Locate and identify every blood parasite.
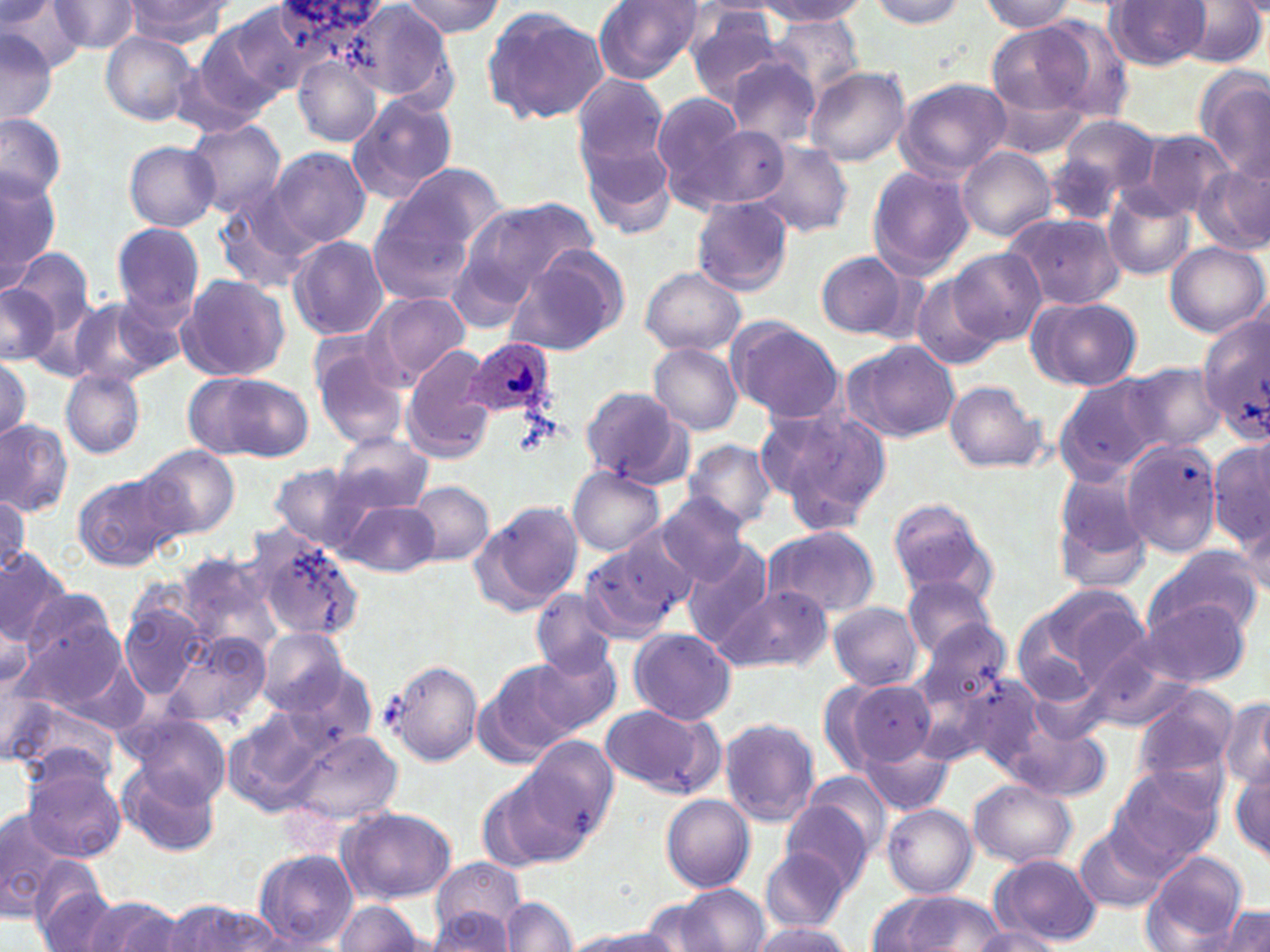

Approximate bounding boxes as [x1, y1, x2, y2] in pixels.
Plasmodium ovale-infected red blood cells: [466, 337, 557, 421].
No Plasmodium falciparum, Plasmodium malariae, Plasmodium vivax, Babesia divergens, or Trypanosoma brucei observed.

Uninfected red blood cell locations: [398, 0, 505, 37], [751, 0, 864, 35], [1106, 0, 1212, 70], [1178, 0, 1266, 69], [2, 1, 87, 74], [48, 1, 141, 56], [124, 1, 230, 46], [866, 1, 968, 29], [978, 1, 1080, 33], [271, 2, 388, 44], [592, 2, 704, 82], [220, 3, 325, 99], [349, 4, 455, 104], [481, 5, 610, 126], [684, 5, 790, 103], [768, 14, 864, 99], [1037, 15, 1138, 123], [196, 20, 295, 119], [985, 24, 1095, 131], [0, 30, 58, 126], [101, 32, 199, 125], [176, 44, 273, 138], [722, 55, 822, 148], [294, 56, 382, 149], [1194, 65, 1270, 181], [804, 66, 910, 168], [569, 72, 669, 177], [893, 77, 1011, 180], [347, 91, 458, 203], [653, 92, 756, 207], [0, 112, 66, 198], [577, 115, 678, 241], [1047, 117, 1162, 219], [184, 120, 287, 218], [693, 126, 790, 208], [1135, 129, 1237, 218], [124, 141, 219, 231], [753, 142, 854, 239], [957, 146, 1056, 242], [269, 148, 370, 248], [385, 161, 510, 254], [1193, 162, 1270, 256], [865, 163, 974, 280], [1, 170, 60, 285], [1103, 186, 1196, 279], [213, 192, 320, 295], [692, 195, 794, 296], [461, 196, 601, 298], [367, 208, 473, 305], [1004, 212, 1125, 311], [111, 221, 206, 324], [288, 235, 389, 341], [1165, 241, 1268, 338], [950, 247, 1045, 346], [504, 248, 627, 355], [11, 249, 94, 335], [817, 251, 910, 341], [640, 266, 746, 357], [909, 273, 1002, 372], [176, 275, 290, 382], [0, 284, 58, 364], [368, 291, 470, 385], [1027, 296, 1142, 391], [69, 298, 162, 385], [1198, 311, 1268, 440], [727, 317, 844, 424], [842, 339, 958, 442], [649, 342, 743, 434], [309, 343, 412, 449], [402, 344, 501, 462], [0, 357, 29, 443], [1127, 360, 1222, 451], [60, 370, 144, 458], [182, 370, 311, 463], [1053, 374, 1171, 484], [942, 379, 1048, 473], [579, 386, 689, 486], [757, 401, 895, 534], [0, 420, 72, 515], [332, 432, 436, 514], [682, 438, 778, 532], [1119, 440, 1223, 558], [1208, 440, 1270, 550], [136, 443, 241, 539], [269, 463, 371, 551], [567, 467, 665, 555], [1049, 468, 1153, 596], [72, 471, 180, 570], [410, 482, 494, 565], [657, 493, 750, 585], [0, 494, 28, 574], [888, 498, 998, 604], [342, 501, 439, 577], [470, 501, 582, 617], [760, 526, 880, 619], [250, 532, 365, 644], [578, 540, 688, 643], [681, 543, 776, 649], [1143, 544, 1266, 641], [0, 548, 73, 645], [179, 554, 281, 659], [901, 575, 997, 660], [714, 584, 834, 673], [21, 590, 121, 684], [531, 590, 619, 677], [1009, 590, 1142, 709], [1141, 597, 1251, 688], [827, 601, 923, 690], [120, 602, 206, 699], [0, 605, 35, 700], [911, 614, 1012, 714], [628, 627, 735, 725], [162, 629, 275, 731], [257, 630, 347, 717], [1078, 642, 1197, 733], [529, 643, 625, 736], [386, 659, 481, 767], [474, 660, 584, 764], [276, 663, 377, 761], [947, 668, 1051, 775], [830, 678, 939, 771], [1132, 686, 1239, 786], [1217, 695, 1270, 794], [9, 698, 116, 778], [599, 703, 722, 797], [227, 707, 335, 813], [120, 709, 231, 805], [719, 717, 821, 826], [1006, 722, 1111, 802], [284, 730, 402, 827], [521, 735, 619, 839], [856, 736, 957, 817], [121, 761, 220, 857], [1230, 762, 1270, 863], [21, 763, 127, 862], [1107, 764, 1224, 869], [794, 771, 892, 868], [477, 775, 578, 872], [967, 779, 1076, 868], [661, 794, 754, 893], [780, 800, 874, 890], [881, 802, 978, 897], [0, 807, 74, 921], [339, 808, 456, 904], [1076, 825, 1170, 913], [759, 846, 850, 933], [252, 849, 357, 948], [988, 853, 1103, 947], [1143, 853, 1249, 948], [431, 856, 528, 945], [27, 863, 119, 952], [655, 886, 770, 952], [869, 892, 1009, 950], [82, 897, 186, 952], [499, 897, 576, 951], [334, 899, 422, 951], [168, 900, 283, 952], [1216, 906, 1270, 952], [426, 909, 515, 950], [749, 920, 856, 950], [967, 927, 1063, 951], [570, 929, 682, 952]. Platelet locations: [513, 413, 557, 457]. Slide-level diagnosis: Plasmodium ovale. Thin blood film. Captured at 1000x magnification. Image is 1270×952 pixels. One field of a larger specimen. May-Grünwald-Giemsa stain. Optical microscopy.